Identify the parasite.
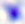

Toxoplasma gondii.

modality = photomicrograph
magnification = 400x